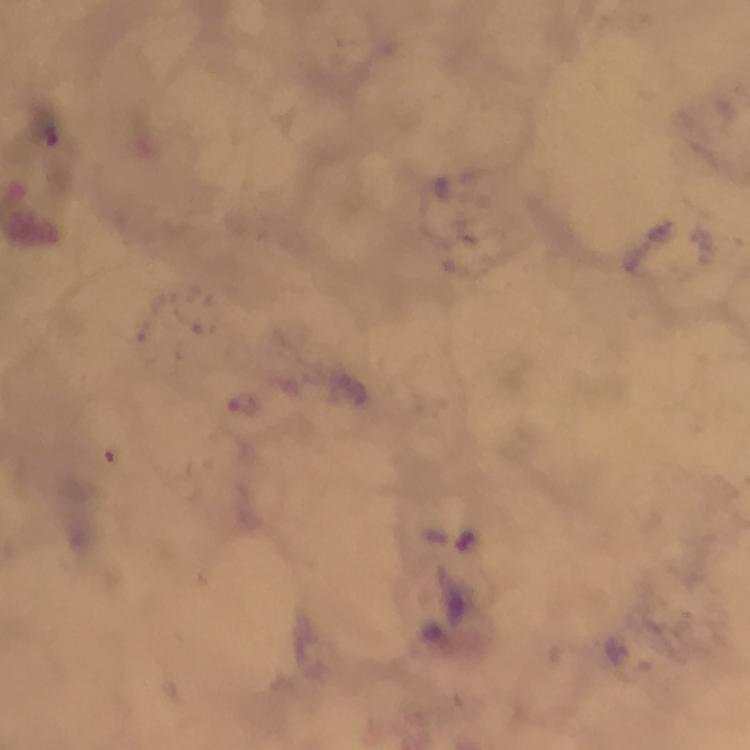
preparation: thick smear
immersion_oil: applied
stain: Giemsa
magnification: 100x
capture: smartphone mounted on the microscope
image_size: 750×750 pixels
malaria_parasite_locations: 'approximate centers as {x, y} in pixels: {242, 406}'
context: from a diagnostic examination for malaria
cropped_from: one field of view